Locate every leukocyte (white blood cell).
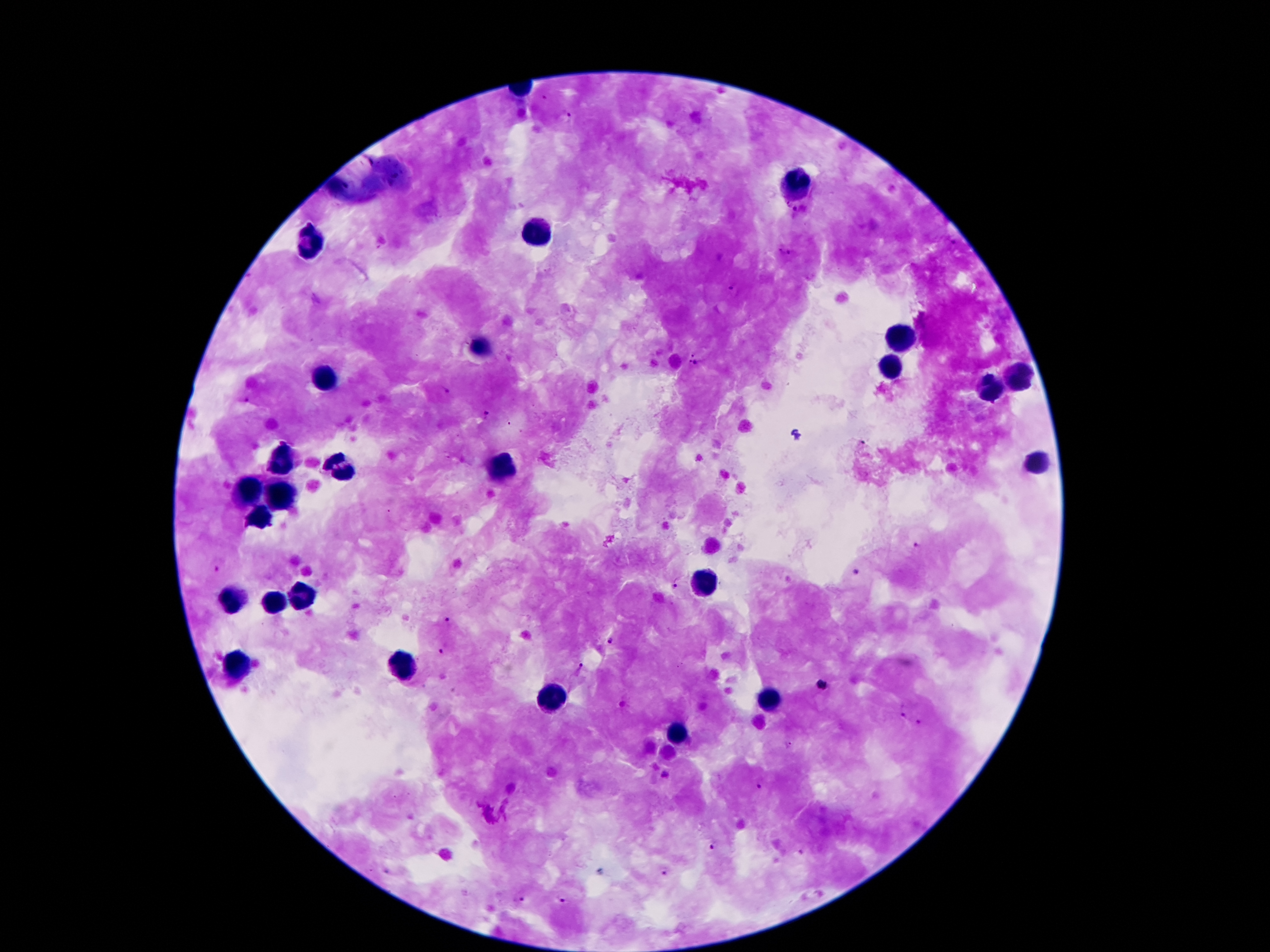
Approximate centers as {x, y} in pixels.
Leukocytes: {798, 184}, {538, 234}, {308, 242}, {896, 339}, {480, 347}, {889, 370}, {326, 378}, {1019, 379}, {995, 390}, {283, 459}, {1034, 465}, {499, 467}, {345, 469}, {250, 491}, {284, 499}, {260, 522}, {705, 582}, {301, 601}, {230, 603}, {273, 604}, {235, 662}, {400, 664}, {551, 701}, {767, 703}, {676, 733}.

Plasmodium parasite locations: {565, 116}, {787, 203}, {794, 210}, {953, 243}, {783, 251}, {734, 289}, {692, 354}, {699, 361}, {689, 363}, {488, 413}, {916, 544}, {217, 569}, {857, 570}, {673, 586}, {449, 620}, {610, 640}, {439, 651}, {576, 670}, {821, 685}, {902, 714}, {917, 723}, {790, 747}, {665, 774}, {759, 786}, {713, 848}, {800, 852}, {663, 873}, {520, 899}, {562, 899}. Photographed through the microscope eyepiece with a smartphone camera. One field from this slide. Image is 1270×952 pixels. Thick blood smear. Patient malaria status: positive for Plasmodium falciparum. 100x magnification. Giemsa-stained preparation.